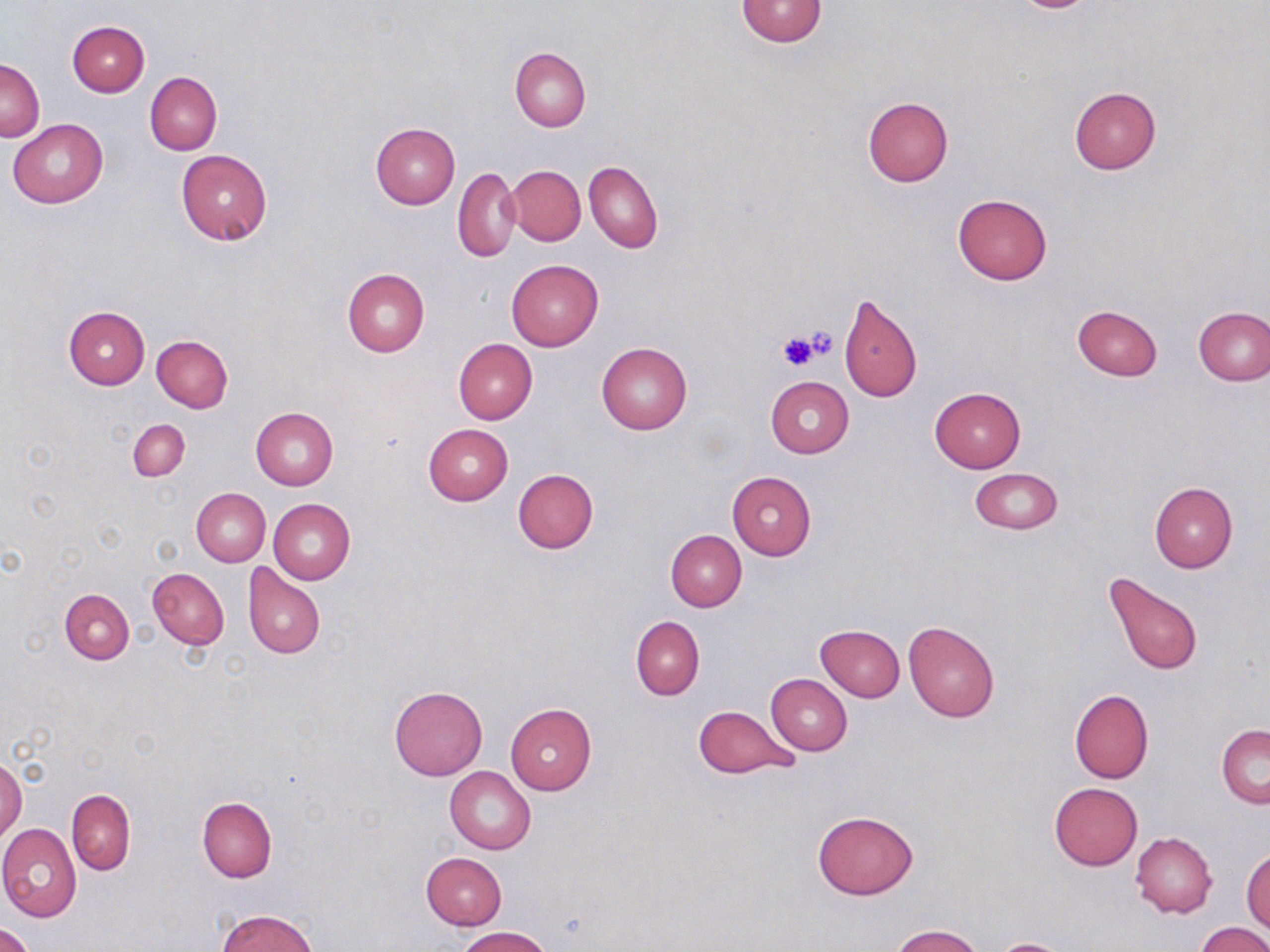
Approximate bounding boxes as [x1, y1, x2, y2] in pixels. Platelet locations: [804, 326, 837, 360], [777, 330, 818, 372]. Uninfected red blood cell locations: [738, 0, 824, 46], [66, 21, 149, 97], [510, 47, 590, 131], [0, 59, 43, 141], [145, 72, 221, 155], [1069, 87, 1160, 175], [863, 95, 953, 186], [8, 118, 108, 208], [370, 122, 460, 209], [176, 150, 273, 244], [584, 161, 662, 254], [507, 165, 586, 246], [453, 168, 521, 262], [953, 193, 1052, 284], [505, 259, 604, 351], [342, 269, 430, 356], [837, 294, 921, 402], [1072, 305, 1163, 381], [63, 306, 150, 389], [1193, 306, 1269, 386], [152, 336, 233, 412], [454, 339, 538, 423], [596, 340, 693, 435], [765, 376, 854, 458], [930, 386, 1026, 472], [250, 407, 338, 490], [128, 418, 190, 481], [423, 424, 513, 505], [968, 468, 1062, 534], [512, 469, 599, 553], [728, 471, 816, 558], [1149, 482, 1237, 573], [191, 487, 271, 567], [268, 498, 356, 584], [666, 529, 746, 612], [242, 562, 325, 660], [147, 567, 229, 649], [1103, 573, 1203, 676], [60, 589, 134, 663], [632, 617, 704, 699], [903, 620, 999, 721], [815, 624, 905, 701], [766, 673, 852, 756], [390, 686, 487, 781], [1070, 688, 1154, 783], [504, 703, 596, 795], [694, 705, 798, 779], [1217, 724, 1270, 809], [0, 757, 24, 844], [445, 766, 536, 854], [1049, 782, 1142, 869], [67, 789, 136, 875], [197, 796, 277, 882], [812, 810, 919, 899], [0, 823, 82, 922], [1130, 831, 1217, 918], [1243, 849, 1270, 933], [421, 853, 505, 930], [218, 908, 317, 952], [1197, 922, 1270, 952], [0, 923, 34, 952], [891, 925, 986, 952], [456, 927, 551, 952]. Slide-level diagnosis: no evidence of blood parasites. Light microscopy. Thin blood smear. Captured at 1000x magnification. Single field of view. May-Grünwald-Giemsa-stained preparation. Image is 1270×952 pixels.